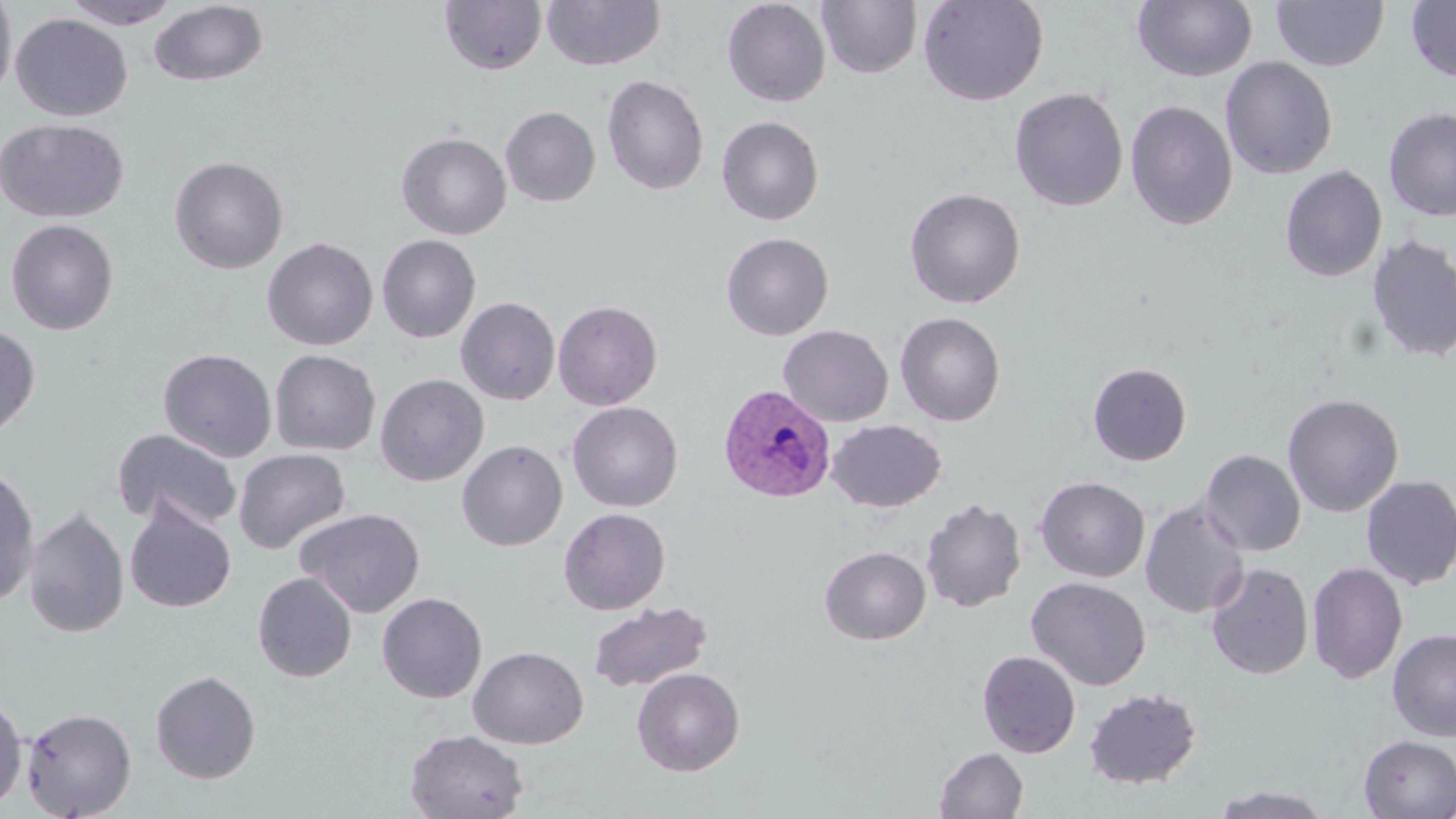
slide-level diagnosis = Plasmodium vivax
magnification = 1000x
uninfected red blood cell locations = approximate bounding boxes as named x1/y1/x2/y2 corners in pixels: (x1=0, y1=0, x2=17, y2=105), (x1=62, y1=0, x2=183, y2=29), (x1=541, y1=0, x2=666, y2=71), (x1=722, y1=0, x2=831, y2=107), (x1=817, y1=0, x2=922, y2=79), (x1=918, y1=0, x2=1049, y2=106), (x1=1131, y1=0, x2=1258, y2=83), (x1=439, y1=1, x2=547, y2=75), (x1=1272, y1=1, x2=1389, y2=71), (x1=1406, y1=1, x2=1456, y2=82), (x1=148, y1=2, x2=269, y2=86), (x1=10, y1=13, x2=133, y2=121), (x1=1220, y1=56, x2=1338, y2=179), (x1=602, y1=75, x2=709, y2=195), (x1=1009, y1=87, x2=1128, y2=211), (x1=1125, y1=100, x2=1238, y2=230), (x1=501, y1=106, x2=601, y2=207), (x1=1383, y1=107, x2=1456, y2=221), (x1=716, y1=116, x2=824, y2=225), (x1=0, y1=118, x2=129, y2=223), (x1=397, y1=132, x2=511, y2=239), (x1=169, y1=156, x2=289, y2=274), (x1=1280, y1=165, x2=1387, y2=282), (x1=904, y1=187, x2=1026, y2=308), (x1=4, y1=218, x2=119, y2=335), (x1=721, y1=232, x2=834, y2=340), (x1=377, y1=234, x2=481, y2=342), (x1=1366, y1=234, x2=1456, y2=363), (x1=262, y1=237, x2=379, y2=350), (x1=456, y1=296, x2=561, y2=405), (x1=553, y1=300, x2=663, y2=410), (x1=895, y1=312, x2=1006, y2=426), (x1=0, y1=322, x2=41, y2=444), (x1=778, y1=324, x2=893, y2=426), (x1=158, y1=347, x2=277, y2=462), (x1=269, y1=349, x2=381, y2=456), (x1=1088, y1=362, x2=1192, y2=465), (x1=375, y1=374, x2=489, y2=486), (x1=1282, y1=393, x2=1403, y2=517), (x1=567, y1=401, x2=683, y2=511), (x1=827, y1=419, x2=946, y2=512), (x1=112, y1=428, x2=241, y2=531), (x1=457, y1=441, x2=567, y2=551), (x1=233, y1=448, x2=351, y2=554), (x1=1200, y1=449, x2=1306, y2=556), (x1=0, y1=464, x2=40, y2=606), (x1=1360, y1=475, x2=1456, y2=589), (x1=1036, y1=476, x2=1150, y2=582), (x1=125, y1=498, x2=237, y2=614), (x1=921, y1=498, x2=1027, y2=613), (x1=1140, y1=499, x2=1250, y2=618), (x1=23, y1=507, x2=129, y2=638), (x1=295, y1=507, x2=426, y2=618), (x1=559, y1=507, x2=670, y2=615), (x1=820, y1=546, x2=931, y2=644), (x1=1307, y1=560, x2=1408, y2=685), (x1=1206, y1=562, x2=1313, y2=680), (x1=252, y1=571, x2=357, y2=683), (x1=1026, y1=577, x2=1151, y2=690), (x1=377, y1=592, x2=487, y2=704), (x1=587, y1=601, x2=713, y2=693), (x1=1387, y1=628, x2=1456, y2=741), (x1=468, y1=645, x2=588, y2=748), (x1=977, y1=650, x2=1081, y2=758), (x1=632, y1=668, x2=745, y2=776), (x1=150, y1=670, x2=261, y2=783), (x1=1084, y1=687, x2=1202, y2=789), (x1=0, y1=692, x2=28, y2=812), (x1=21, y1=707, x2=137, y2=819), (x1=405, y1=729, x2=529, y2=818), (x1=1358, y1=735, x2=1456, y2=818), (x1=934, y1=747, x2=1028, y2=818), (x1=1211, y1=785, x2=1335, y2=818)
stain = May-Grünwald-Giemsa
preparation = thin blood film
modality = optical microscopy
image size = 1456×819 pixels
Plasmodium vivax-infected red blood cell locations = approximate bounding boxes as named x1/y1/x2/y2 corners in pixels: (x1=718, y1=384, x2=836, y2=504)
field of view = one of a larger specimen